Identify the parasite.
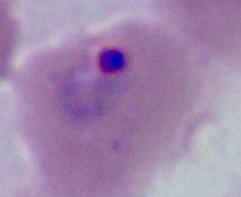

Plasmodium.

Summary:
  - Modality: photomicrograph
  - Magnification: 400x or 1000x